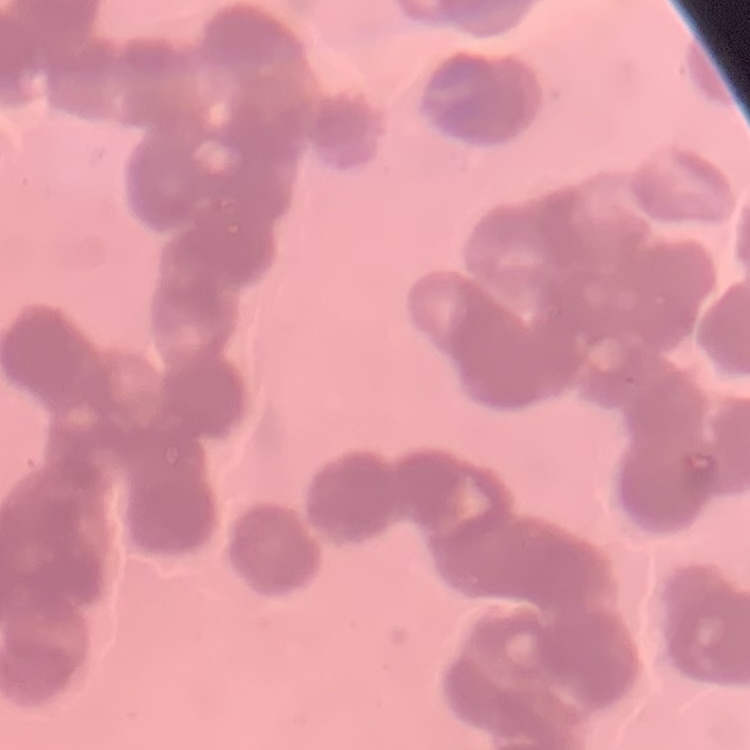 The red blood cells exhibit rouleaux formation. One tile cut from a larger photomicrograph. Field's or Giemsa stain. Thin peripheral smear.